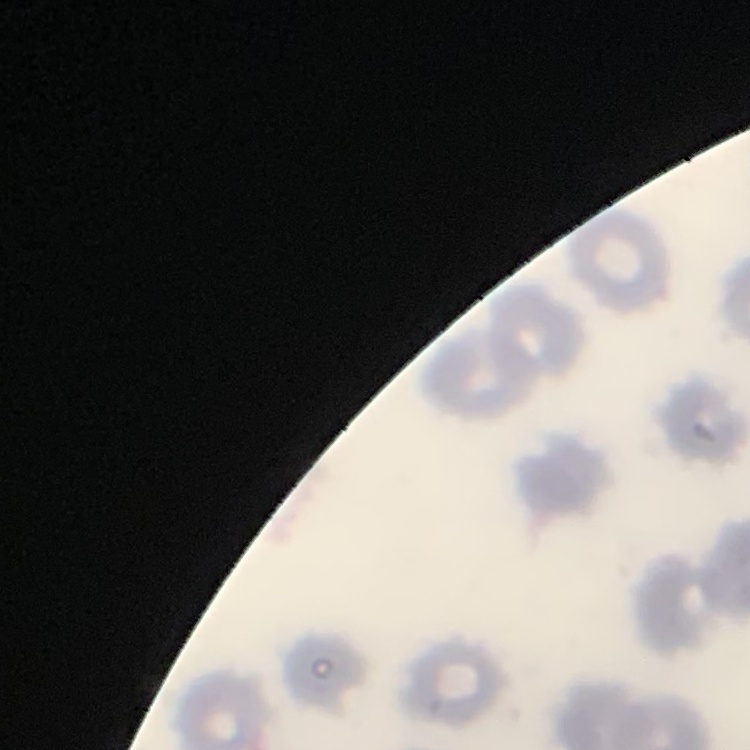
red blood cell morphology = no rouleaux formation
image type = square crop of a larger photomicrograph
preparation = thin blood smear
stain = Field's or Giemsa